Classify this cell by malaria status.
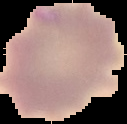
It is uninfected.

{
  "preparation": "thin blood smear",
  "image_type": "segmented cell region with the area outside set to black",
  "image_size": "127×124 pixels"
}